Give the preparation type.
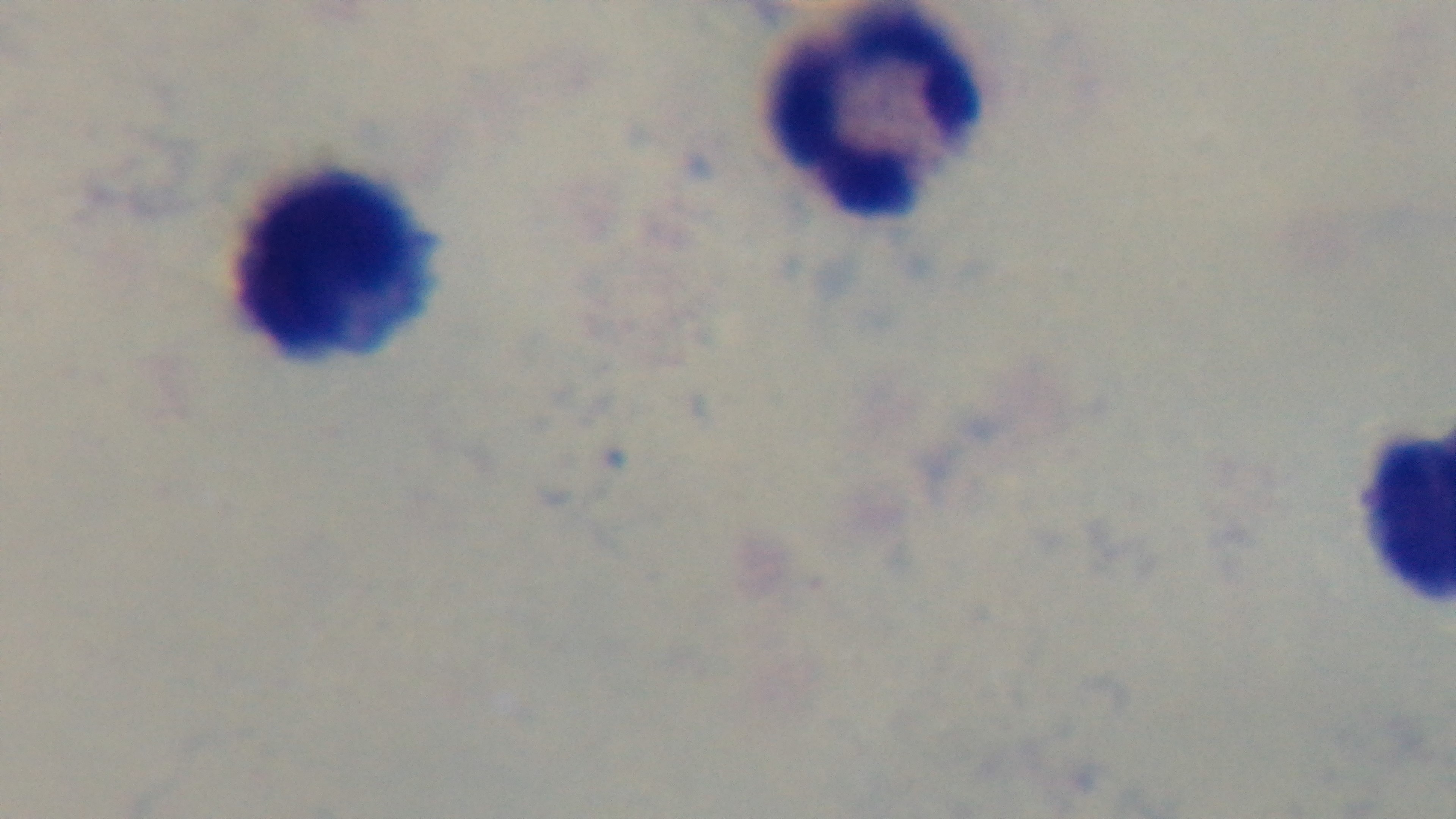
Thick.

Malaria status: negative. Giemsa stain. One field from the slide. Oil-immersion objective, 100x. Light microscopy. Captured with a mounted 4K digital camera.